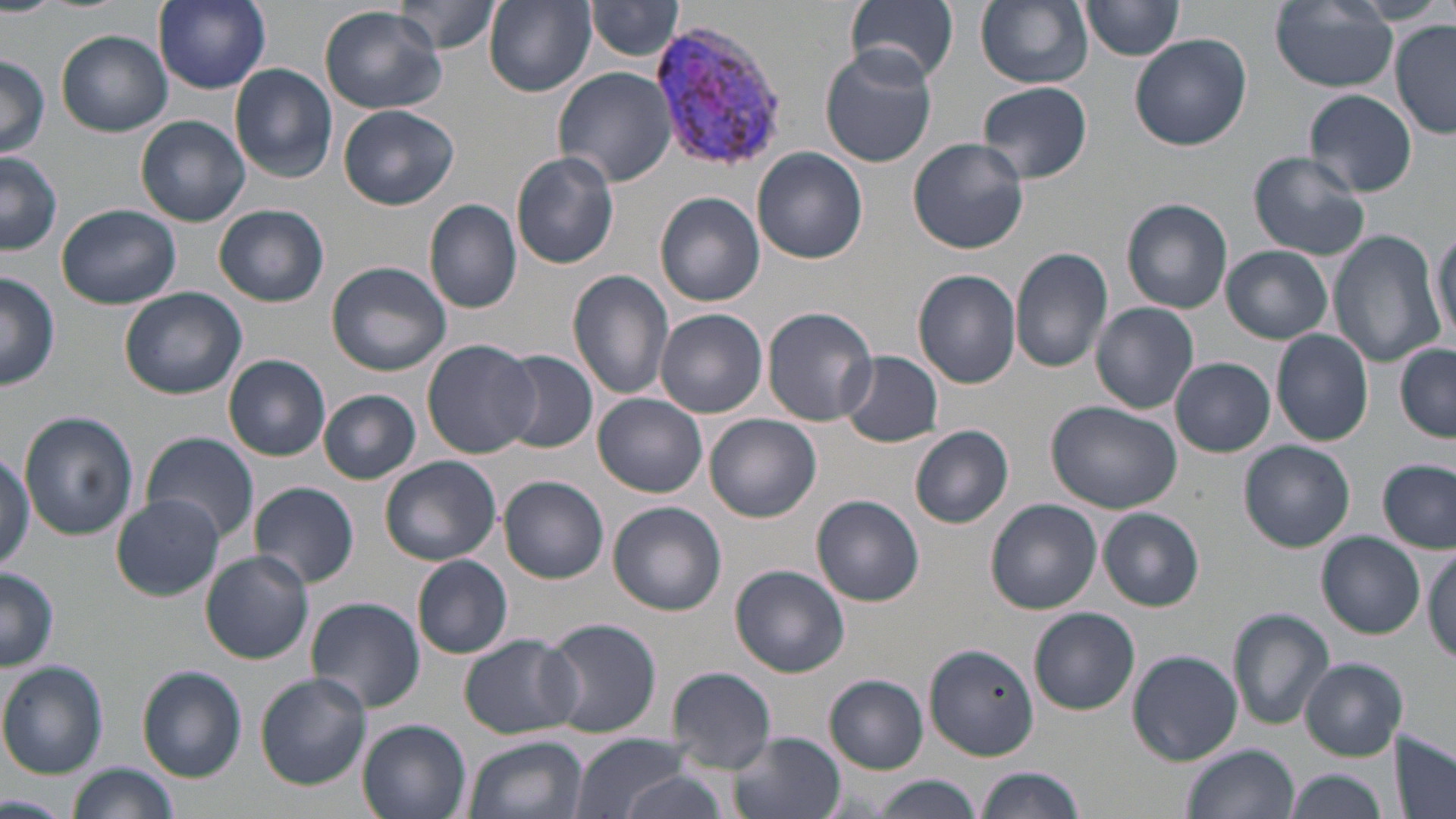
Summary:
  - Coordinate format: approximate bounding boxes as named x1/y1/x2/y2 corners in pixels
  - Uninfected red blood cell locations: (x1=153, y1=0, x2=271, y2=92), (x1=392, y1=0, x2=502, y2=55), (x1=485, y1=0, x2=596, y2=96), (x1=976, y1=0, x2=1093, y2=89), (x1=1080, y1=0, x2=1187, y2=60), (x1=587, y1=1, x2=685, y2=61), (x1=1271, y1=1, x2=1399, y2=91), (x1=845, y1=2, x2=960, y2=83), (x1=320, y1=4, x2=446, y2=114), (x1=1391, y1=20, x2=1456, y2=138), (x1=57, y1=29, x2=172, y2=136), (x1=1130, y1=33, x2=1251, y2=151), (x1=819, y1=45, x2=940, y2=169), (x1=0, y1=56, x2=48, y2=160), (x1=230, y1=63, x2=338, y2=182), (x1=554, y1=67, x2=677, y2=186), (x1=977, y1=80, x2=1093, y2=185), (x1=1304, y1=88, x2=1417, y2=197), (x1=339, y1=104, x2=460, y2=211), (x1=137, y1=114, x2=250, y2=226), (x1=908, y1=137, x2=1029, y2=255), (x1=753, y1=147, x2=868, y2=264), (x1=0, y1=151, x2=61, y2=255), (x1=1249, y1=151, x2=1370, y2=261), (x1=511, y1=152, x2=620, y2=269), (x1=655, y1=191, x2=766, y2=307), (x1=1122, y1=197, x2=1234, y2=314), (x1=424, y1=198, x2=524, y2=315), (x1=213, y1=203, x2=329, y2=307), (x1=58, y1=205, x2=180, y2=308), (x1=1431, y1=224, x2=1455, y2=343), (x1=1329, y1=230, x2=1444, y2=367), (x1=1009, y1=245, x2=1115, y2=374), (x1=1221, y1=245, x2=1333, y2=344), (x1=326, y1=261, x2=452, y2=376), (x1=566, y1=269, x2=675, y2=401), (x1=1, y1=271, x2=61, y2=389), (x1=915, y1=271, x2=1022, y2=390), (x1=118, y1=287, x2=247, y2=400), (x1=1091, y1=302, x2=1199, y2=414), (x1=764, y1=307, x2=880, y2=427), (x1=657, y1=310, x2=768, y2=419), (x1=1270, y1=328, x2=1375, y2=446), (x1=423, y1=338, x2=540, y2=459), (x1=1395, y1=345, x2=1456, y2=443), (x1=498, y1=349, x2=599, y2=454), (x1=837, y1=351, x2=943, y2=448), (x1=223, y1=355, x2=332, y2=462), (x1=1170, y1=357, x2=1276, y2=457), (x1=318, y1=388, x2=422, y2=485), (x1=593, y1=393, x2=708, y2=497), (x1=1046, y1=400, x2=1181, y2=514), (x1=20, y1=411, x2=138, y2=540), (x1=705, y1=413, x2=821, y2=523), (x1=909, y1=425, x2=1014, y2=529), (x1=141, y1=432, x2=259, y2=541), (x1=1241, y1=439, x2=1355, y2=551), (x1=0, y1=446, x2=36, y2=571), (x1=378, y1=457, x2=501, y2=567), (x1=1378, y1=459, x2=1456, y2=553), (x1=499, y1=476, x2=610, y2=583), (x1=248, y1=480, x2=359, y2=588), (x1=111, y1=495, x2=225, y2=600), (x1=812, y1=495, x2=925, y2=606), (x1=986, y1=499, x2=1101, y2=616), (x1=607, y1=501, x2=727, y2=615), (x1=1099, y1=509, x2=1204, y2=611), (x1=1317, y1=533, x2=1426, y2=638), (x1=1425, y1=546, x2=1456, y2=663), (x1=201, y1=551, x2=314, y2=664), (x1=411, y1=553, x2=513, y2=659), (x1=731, y1=564, x2=849, y2=676), (x1=0, y1=567, x2=60, y2=670), (x1=305, y1=596, x2=425, y2=713), (x1=1229, y1=607, x2=1334, y2=731), (x1=1029, y1=608, x2=1140, y2=716), (x1=543, y1=617, x2=661, y2=739), (x1=460, y1=635, x2=581, y2=738), (x1=924, y1=643, x2=1041, y2=759), (x1=1128, y1=649, x2=1243, y2=766), (x1=1299, y1=658, x2=1408, y2=760), (x1=0, y1=662, x2=108, y2=777), (x1=138, y1=666, x2=248, y2=781), (x1=666, y1=667, x2=777, y2=774), (x1=256, y1=674, x2=371, y2=790), (x1=825, y1=675, x2=929, y2=773), (x1=356, y1=718, x2=472, y2=819), (x1=569, y1=731, x2=692, y2=819), (x1=731, y1=733, x2=846, y2=819), (x1=1389, y1=733, x2=1455, y2=819), (x1=463, y1=734, x2=587, y2=819), (x1=1180, y1=743, x2=1299, y2=819), (x1=67, y1=763, x2=177, y2=819), (x1=976, y1=767, x2=1084, y2=819), (x1=1284, y1=768, x2=1389, y2=819), (x1=614, y1=772, x2=732, y2=819), (x1=876, y1=776, x2=982, y2=817), (x1=0, y1=793, x2=66, y2=818)
  - Plasmodium vivax-infected red blood cell locations: (x1=649, y1=18, x2=786, y2=173)
  - Slide-level diagnosis: Plasmodium vivax
  - Modality: optical microscopy
  - Field of view: one of a larger specimen
  - Magnification: 1000x
  - Stain: May-Grünwald-Giemsa
  - Preparation: thin blood smear
  - Image size: 1456×819 pixels